Point out each Plasmodium parasite.
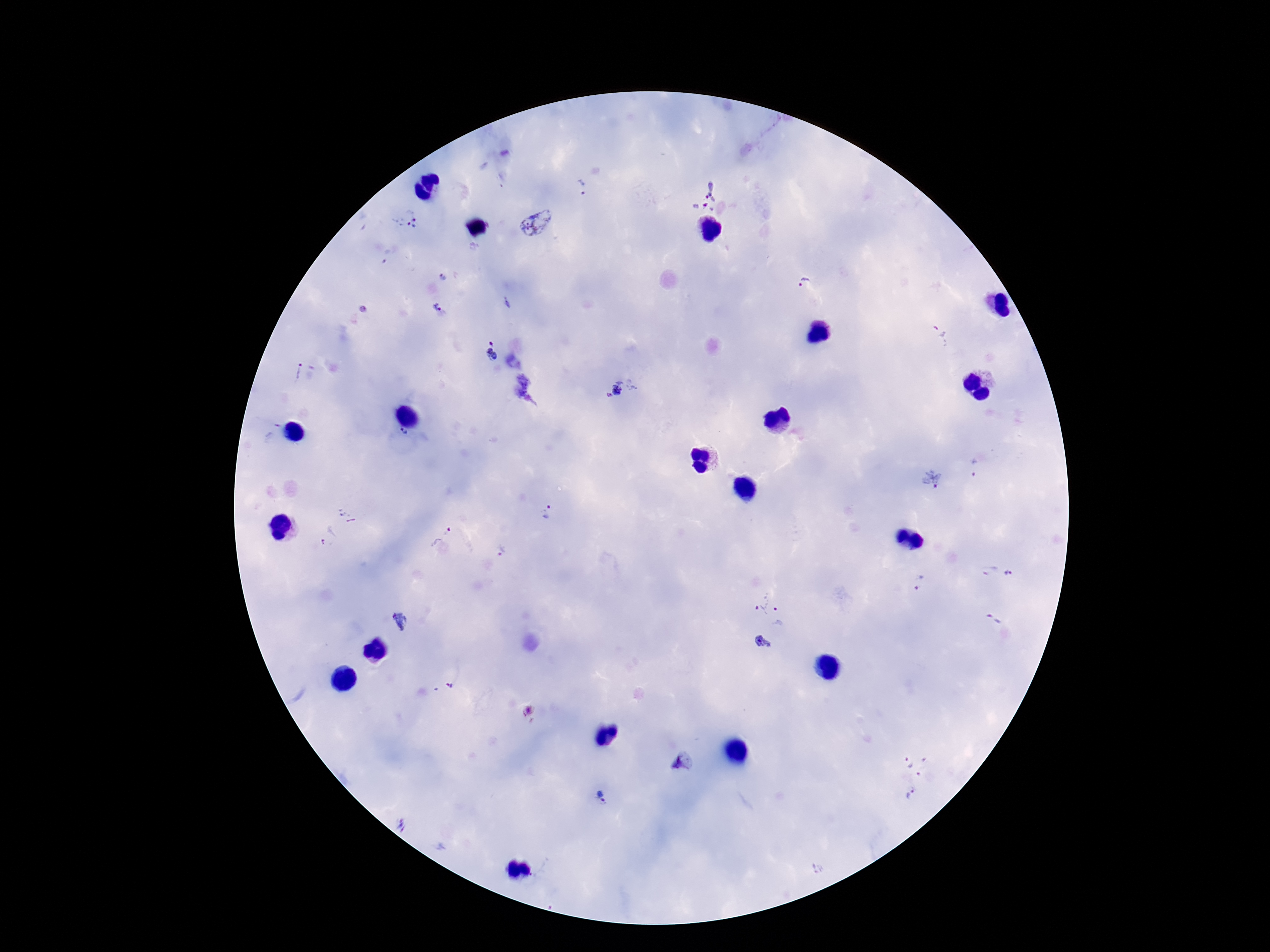
Approximate object centers, in pixels from the top-left corner.
Plasmodium parasites: (x=582, y=186), (x=709, y=196), (x=405, y=220), (x=537, y=222), (x=443, y=278), (x=805, y=284), (x=506, y=302), (x=437, y=307), (x=941, y=334), (x=492, y=349), (x=294, y=371), (x=622, y=388), (x=403, y=436), (x=975, y=468), (x=931, y=480), (x=549, y=513), (x=347, y=515), (x=441, y=534), (x=329, y=537), (x=502, y=552), (x=990, y=571), (x=1009, y=574), (x=919, y=583), (x=759, y=602), (x=781, y=615), (x=994, y=619), (x=404, y=624), (x=761, y=642), (x=450, y=686), (x=530, y=711), (x=682, y=764), (x=912, y=777), (x=602, y=797), (x=404, y=825).

Summary:
  - Preparation: thick peripheral-blood smear
  - Stain: Giemsa
  - Image size: 1270×952 pixels
  - Patient malaria status: positive
  - Capture: smartphone camera through the microscope eyepiece
  - Magnification: 100x
  - Field of view: single